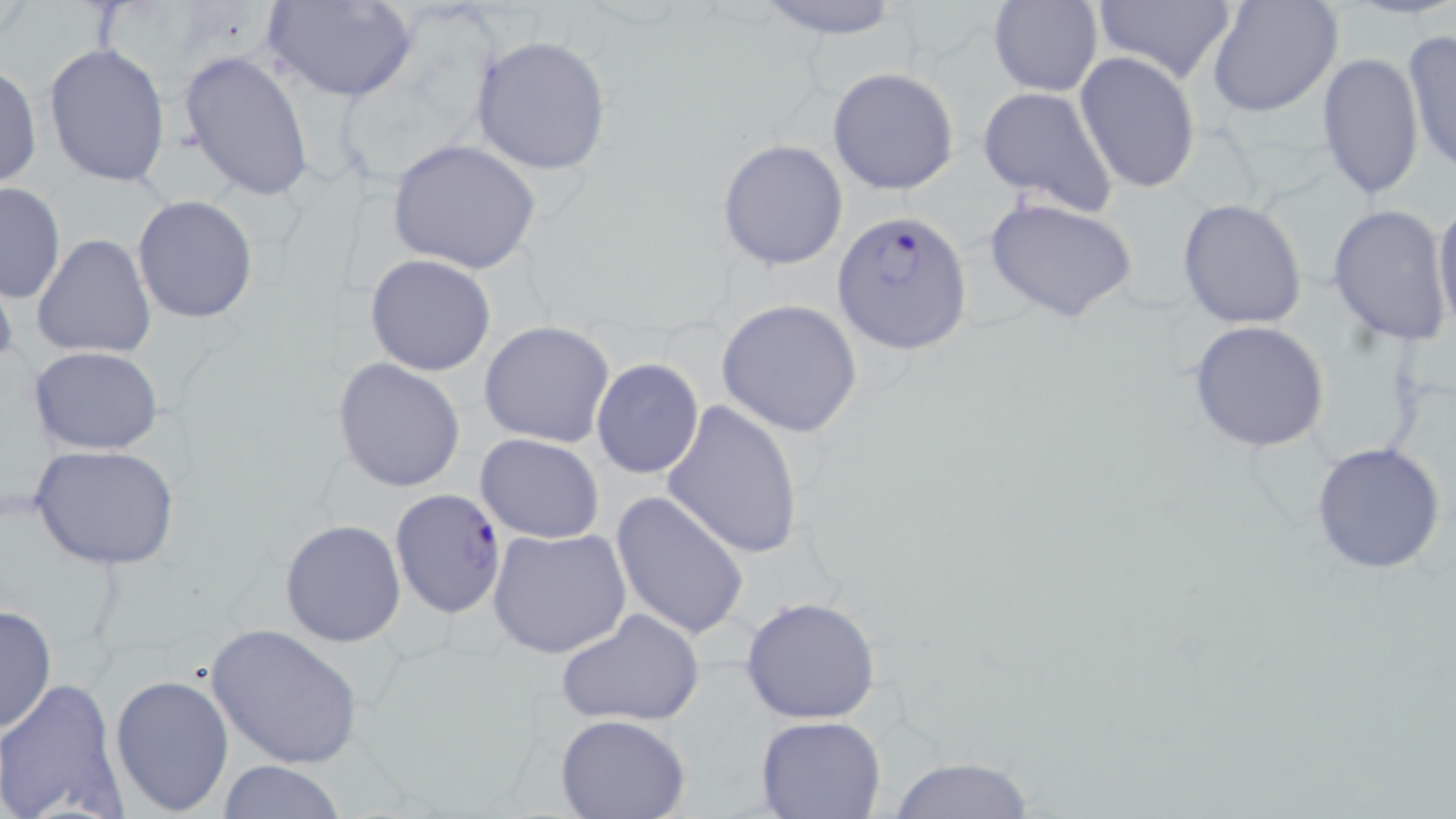

Summary:
  - Coordinate format: approximate bounding boxes as (x1,y1)-(x2,y2) corner pairs in pixels
  - Uninfected red blood cell locations: (268,0)-(418,103), (749,0)-(909,40), (1088,0)-(1240,87), (1205,0)-(1344,119), (988,1)-(1103,96), (1402,31)-(1455,173), (470,34)-(611,175), (43,41)-(171,188), (178,50)-(315,202), (1073,51)-(1202,196), (1316,52)-(1425,200), (0,67)-(41,190), (827,67)-(959,196), (976,86)-(1120,217), (718,138)-(848,271), (386,139)-(539,274), (0,182)-(65,303), (131,195)-(259,324), (984,195)-(1140,324), (1432,195)-(1456,335), (1176,198)-(1307,330), (1326,204)-(1453,346), (32,235)-(156,360), (366,254)-(496,375), (0,266)-(19,384), (715,298)-(864,437), (480,320)-(617,449), (1188,320)-(1332,453), (500,341)-(688,469), (28,345)-(164,454), (332,356)-(466,492), (591,357)-(705,479), (659,400)-(805,558), (476,432)-(604,543), (1309,441)-(1448,577), (30,444)-(181,572), (610,492)-(750,640), (280,519)-(405,647), (487,527)-(631,658), (739,596)-(883,723), (0,604)-(57,736), (555,607)-(705,730), (204,622)-(366,770), (109,673)-(236,814), (0,676)-(130,819), (555,714)-(693,819), (756,715)-(887,819), (888,755)-(1036,819), (216,759)-(346,818)
  - Plasmodium falciparum-infected red blood cell locations: (833,208)-(974,356), (389,488)-(508,620)
  - Slide-level diagnosis: Plasmodium falciparum
  - Modality: light microscopy
  - Preparation: thin blood film
  - Stain: May-Grünwald-Giemsa
  - Magnification: 1000x
  - Field of view: one of a larger specimen
  - Image size: 1456×819 pixels